Outline each blood parasite and name the species.
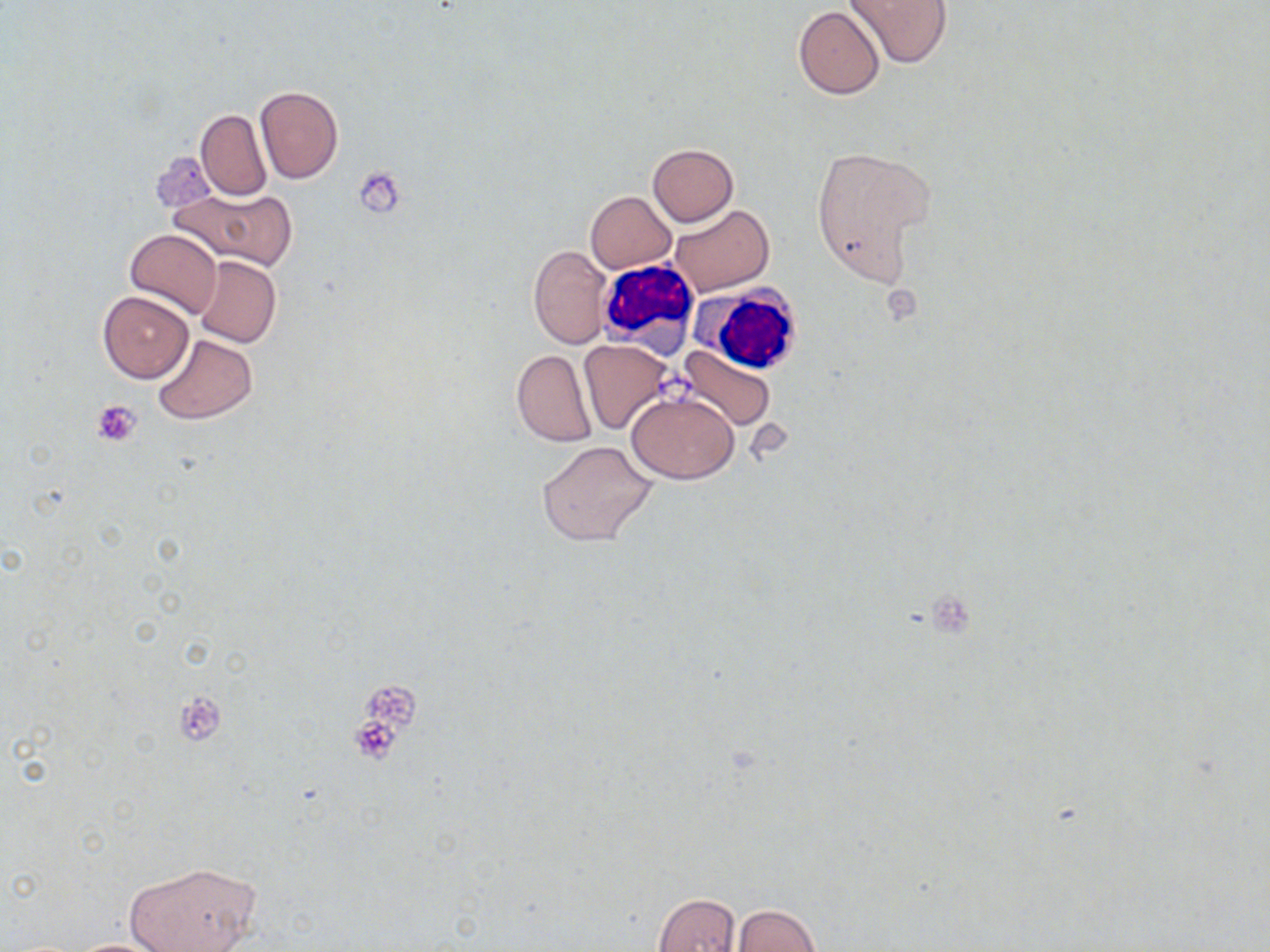
No blood parasites seen.

Approximate bounding boxes as [x1, y1, x2, y2] in pixels. Uninfected red blood cell locations: [843, 0, 951, 69], [793, 5, 885, 98], [254, 85, 342, 183], [195, 110, 271, 200], [647, 144, 739, 226], [810, 145, 936, 287], [168, 184, 296, 272], [585, 191, 676, 273], [671, 204, 773, 296], [125, 228, 221, 318], [527, 244, 612, 349], [194, 255, 281, 347], [98, 290, 194, 383], [152, 334, 257, 424], [578, 339, 674, 435], [676, 345, 776, 432], [511, 350, 597, 447], [627, 391, 738, 484], [536, 440, 659, 548], [122, 860, 260, 951], [653, 892, 741, 952], [730, 904, 822, 952], [60, 937, 179, 951]. White blood cell locations: [597, 258, 696, 361], [688, 283, 806, 374]. Platelet locations: [353, 171, 413, 218], [94, 400, 143, 445], [927, 586, 971, 636], [345, 682, 422, 763], [174, 691, 227, 747]. Slide-level diagnosis: negative for blood parasites. Image is 1270×952 pixels. 1000x magnification. Light microscopy. One field of a larger specimen. Thin blood film. May-Grünwald-Giemsa stain.